Give the position of every Plasmodium parasite.
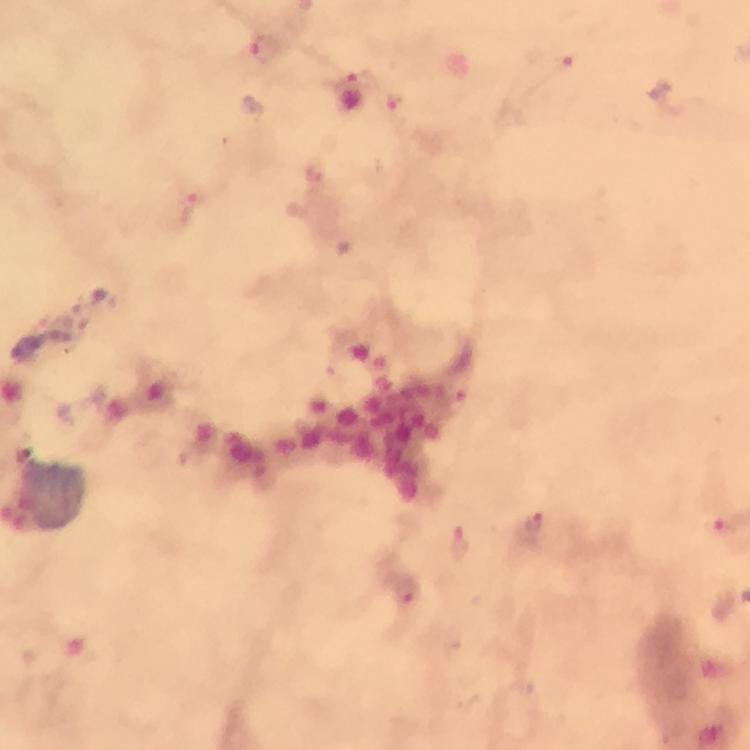

Approximate centers as {x, y} in pixels.
Plasmodium parasites: {263, 49}, {562, 57}, {354, 81}, {399, 100}, {191, 211}, {531, 525}, {723, 525}, {460, 541}.

Summary:
  - Image size: 750×750 pixels
  - Stain: Giemsa
  - Magnification: 100x
  - Capture: smartphone mounted on the microscope
  - Context: from a diagnostic examination for malaria
  - Cropped from: a single field of view
  - Preparation: thick blood smear
  - Immersion oil: used